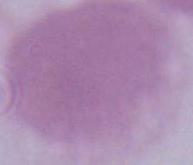

identification = erythrocyte
magnification = 1000x
modality = photomicrograph